Identify the preparation type.
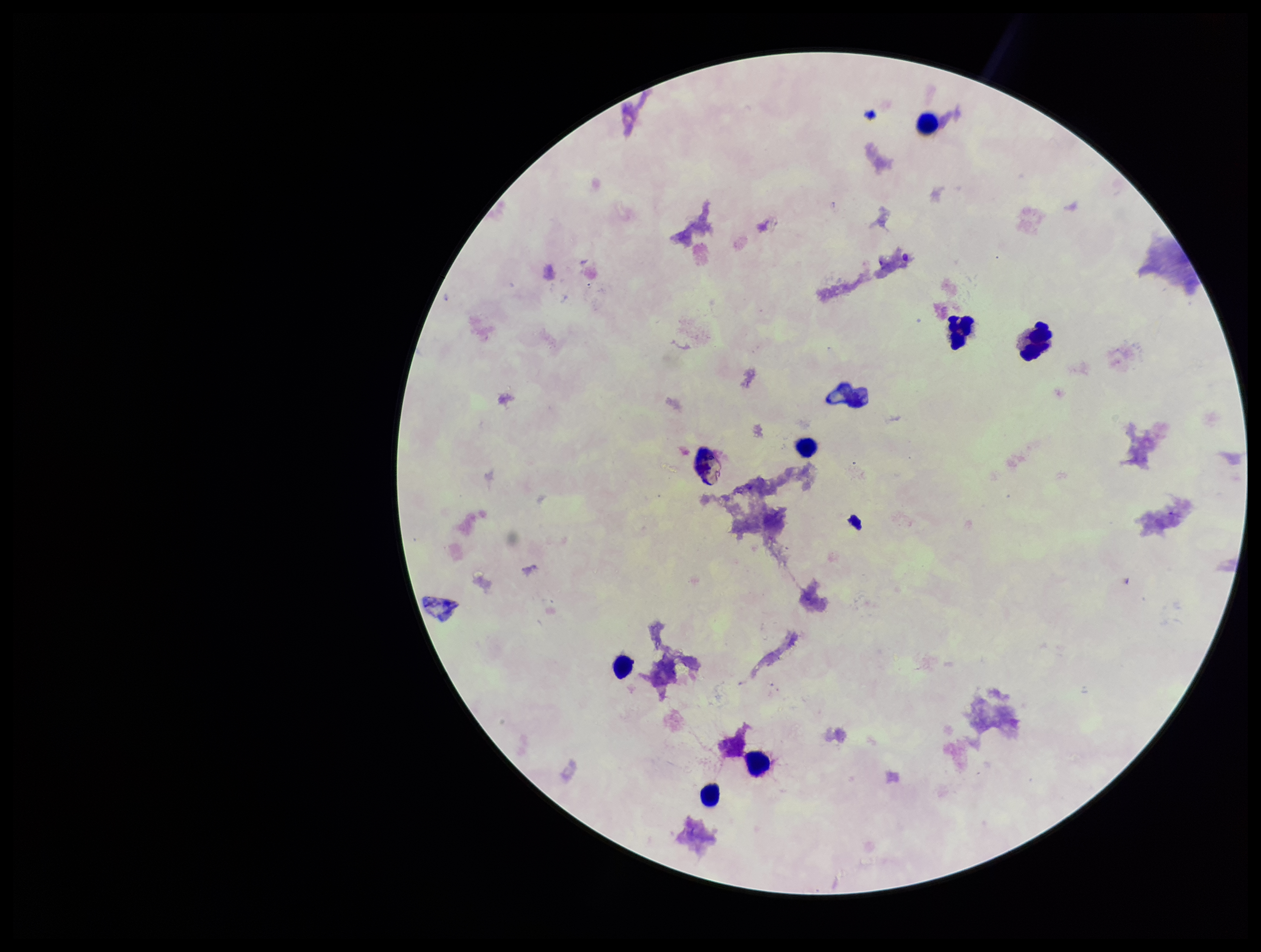
A thick smear.

Summary:
  - Image size: 1261×952 pixels
  - Leukocyte count: 7
  - Parasite count: 0
  - Capture: smartphone photograph through the microscope eyepiece
  - Patient malaria status: negative
  - Field of view: one from this slide
  - Plasmodium parasites: none seen
  - Stain: Giemsa